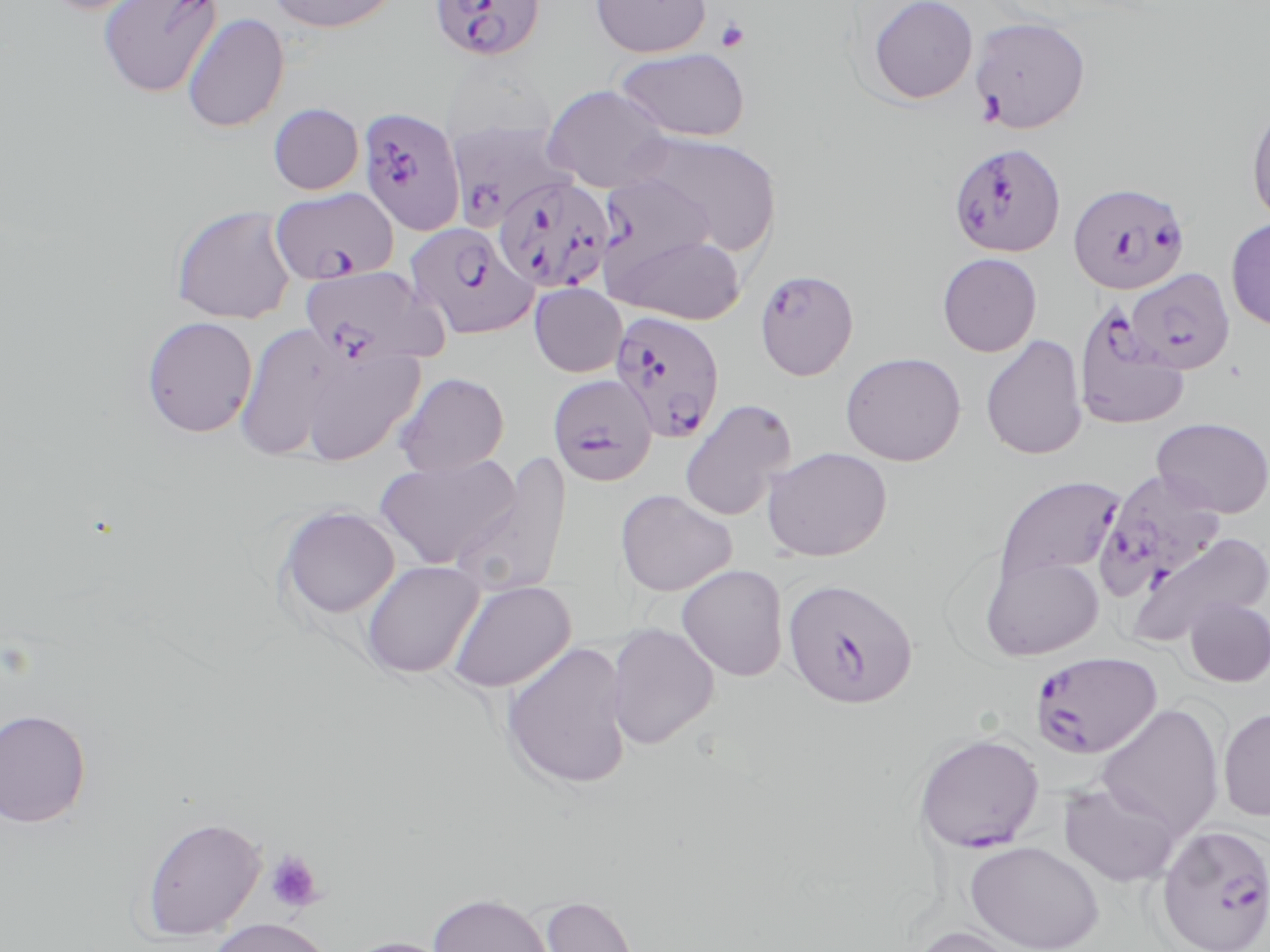
slide-level diagnosis = Plasmodium falciparum
magnification = 1000x
field of view = one of a larger specimen
uninfected red blood cell locations = approximate bounding boxes as (x1, y1, x2, y2) in pixels: (38, 0, 168, 15), (98, 0, 224, 98), (266, 0, 400, 33), (590, 0, 712, 57), (867, 0, 978, 104), (182, 13, 289, 133), (969, 16, 1091, 133), (614, 47, 751, 141), (542, 85, 674, 193), (1246, 100, 1270, 228), (268, 103, 363, 195), (627, 130, 782, 255), (599, 173, 716, 278), (171, 206, 296, 324), (1226, 218, 1270, 331), (606, 234, 745, 324), (937, 252, 1042, 357), (529, 283, 627, 377), (140, 316, 258, 438), (233, 321, 343, 461), (980, 334, 1088, 460), (300, 347, 425, 466), (840, 352, 966, 466), (394, 372, 510, 476), (678, 398, 796, 522), (1151, 416, 1270, 517), (761, 446, 893, 561), (449, 453, 573, 601), (375, 454, 522, 570), (615, 489, 737, 596), (276, 505, 401, 619), (1126, 530, 1270, 649), (980, 554, 1105, 659), (362, 559, 484, 679), (676, 564, 788, 681), (446, 579, 576, 693), (1183, 595, 1270, 687), (605, 622, 721, 749), (507, 639, 640, 789), (1095, 703, 1225, 839), (1218, 706, 1270, 822), (0, 708, 92, 827), (1058, 780, 1182, 887), (140, 816, 265, 940), (965, 840, 1105, 951), (428, 892, 553, 952), (540, 894, 642, 952), (204, 916, 336, 952), (909, 924, 1032, 952), (336, 935, 462, 952)
modality = light microscopy
image size = 1270×952 pixels
preparation = thin blood smear
Plasmodium falciparum-infected red blood cell locations = approximate bounding boxes as (x1, y1, x2, y2) in pixels: (430, 0, 546, 61), (357, 106, 466, 236), (448, 120, 575, 231), (948, 142, 1066, 258), (492, 176, 614, 295), (1067, 182, 1191, 294), (271, 187, 398, 284), (404, 222, 537, 340), (298, 266, 447, 369), (754, 268, 859, 381), (1126, 268, 1236, 374), (1073, 302, 1191, 431), (609, 310, 726, 442), (547, 374, 658, 486), (1094, 470, 1228, 598), (992, 475, 1127, 594), (782, 577, 919, 709), (1031, 650, 1162, 759), (914, 733, 1043, 854), (1155, 824, 1270, 952)
stain = May-Grünwald-Giemsa
platelet locations = approximate bounding boxes as (x1, y1, x2, y2) in pixels: (715, 18, 750, 53), (264, 850, 324, 913)